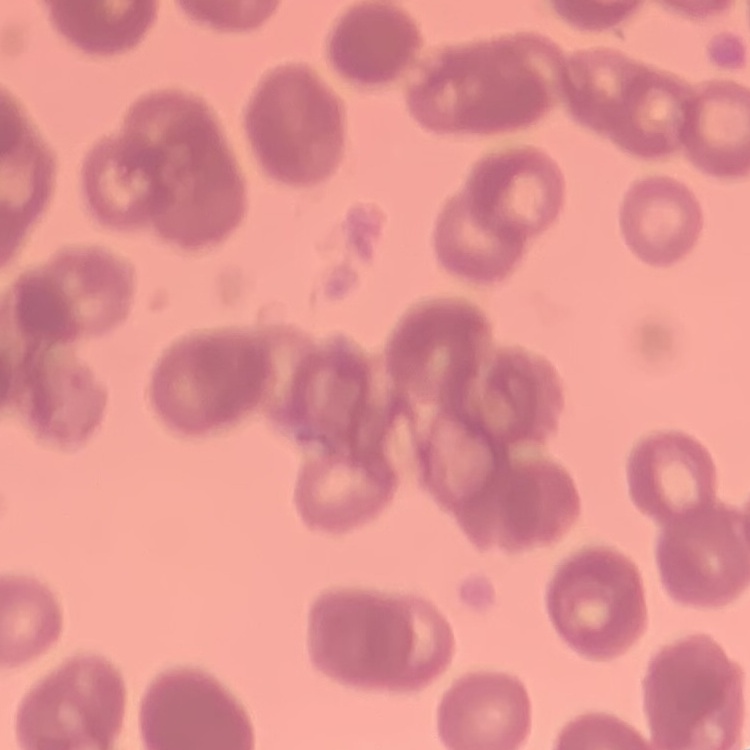 The erythrocytes show rouleaux formation. One tile cut from a larger photomicrograph. Field's or Giemsa stain. Thin peripheral smear.